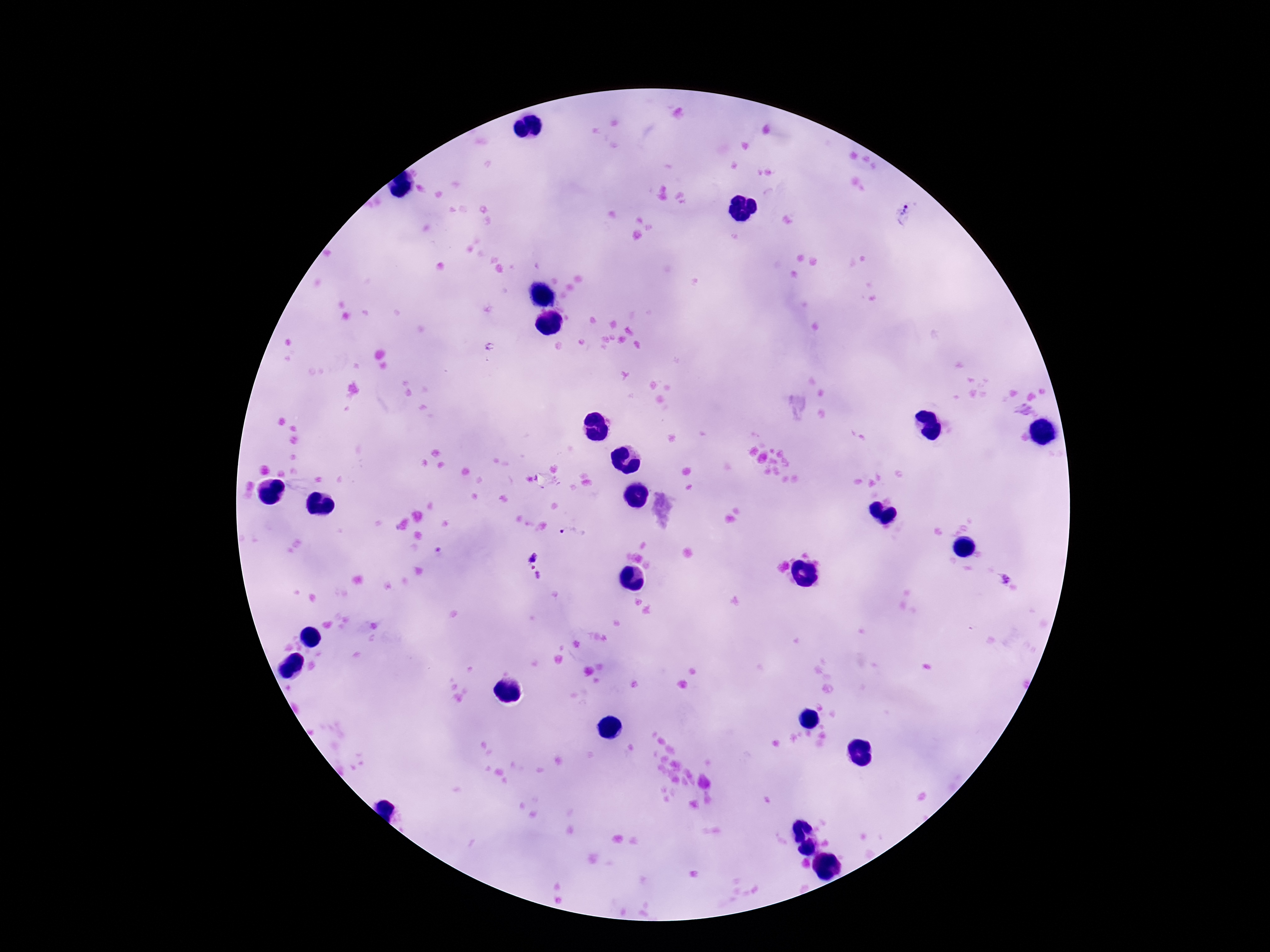

Approximate object centers, in pixels from the top-left corner. Plasmodium parasite locations: (x=903, y=212), (x=1027, y=413), (x=571, y=534), (x=534, y=558), (x=535, y=574), (x=1003, y=577). Image is 1270×952 pixels. Thick blood smear. Patient malaria status: infected. Single field of view. Smartphone photograph taken through the microscope eyepiece. 100x magnification. Giemsa-stained preparation.